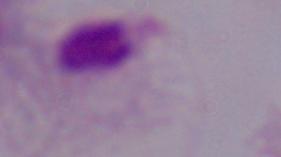

A trichomonad is seen. 1000x magnification. Micrograph.